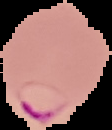

Summary:
  - Image size: 112×130 pixels
  - Image type: segmented cell region with the area outside set to black
  - Malaria status: parasitized
  - Preparation: thin blood film